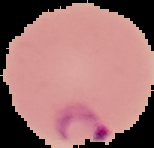 Segmented cell region on a black background. Result: Plasmodium parasites detected. Image is 154×148 pixels. From a thin blood film.